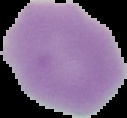

malaria status = uninfected
image type = segmented cell region on a black background
image size = 127×118 pixels
preparation = thin blood film